Look for parasitized red blood cells.
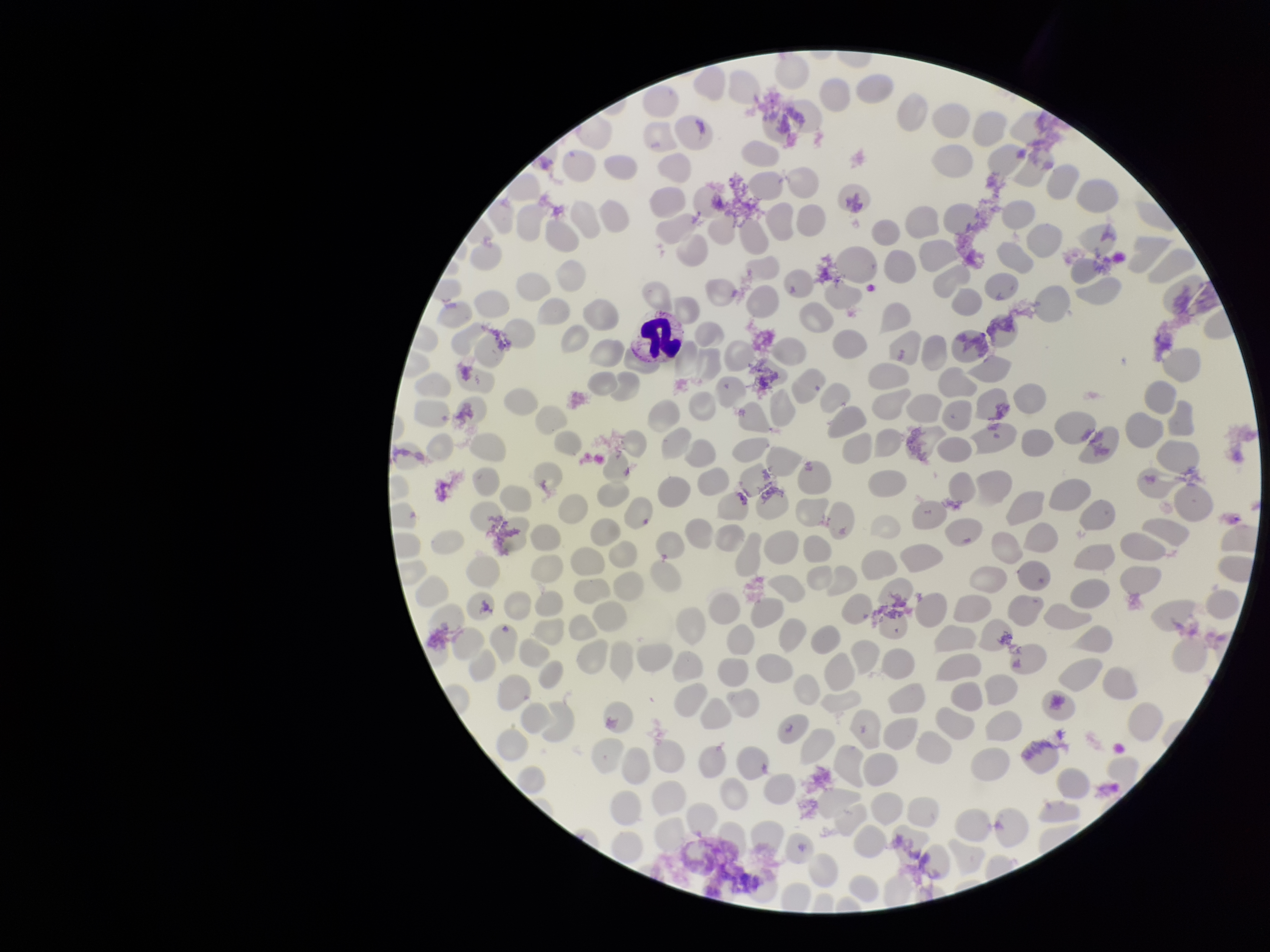

None seen.

{
  "image_size": "1270×952 pixels",
  "field_of_view": "single",
  "red_blood_cell_count": 268,
  "stain": "Giemsa",
  "capture": "smartphone photograph through the microscope eyepiece",
  "parasitized_red_blood_cell_count": 0,
  "preparation": "thin",
  "patient_malaria_status": "negative"
}